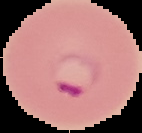
{
  "preparation": "thin blood film",
  "image_size": "142×133 pixels",
  "result": "Plasmodium parasites detected",
  "image_type": "segmented cell region on a black background"
}